Identify the blood parasite species.
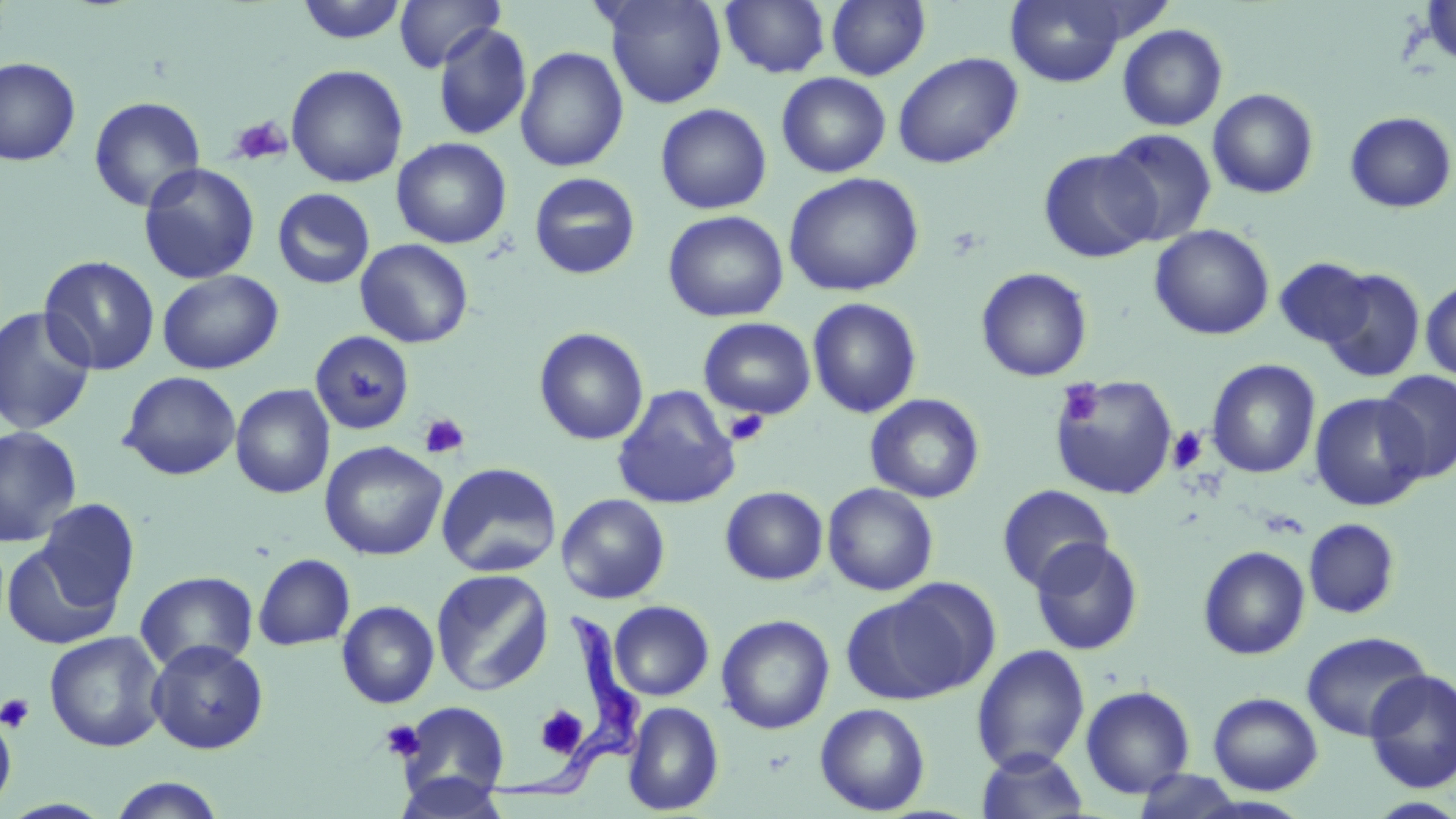

Trypanosoma brucei.

image size = 1456×819 pixels
magnification = 1000x
Trypanosoma brucei locations = approximate bounding boxes as (x1, y1, x2, y2) in pixels: (484, 610, 647, 804)
platelet locations = approximate bounding boxes as (x1, y1, x2, y2) in pixels: (227, 115, 292, 167), (1058, 380, 1104, 426), (724, 409, 770, 447), (418, 413, 469, 460), (1167, 427, 1208, 473), (0, 693, 36, 734), (535, 705, 588, 758), (380, 719, 426, 762)
stain = May-Grünwald-Giemsa
uninfected red blood cell locations = approximate bounding boxes as (x1, y1, x2, y2) in pixels: (394, 0, 504, 72), (601, 0, 728, 108), (720, 0, 831, 78), (826, 0, 930, 81), (1004, 0, 1130, 87), (1420, 0, 1456, 70), (295, 1, 409, 45), (432, 22, 532, 141), (1117, 24, 1228, 131), (515, 46, 629, 173), (893, 52, 1022, 169), (0, 57, 81, 166), (286, 64, 409, 188), (776, 72, 890, 178), (1207, 88, 1319, 199), (88, 95, 206, 212), (655, 103, 772, 215), (1343, 111, 1455, 213), (1102, 128, 1218, 246), (391, 137, 512, 249), (1038, 148, 1160, 263), (138, 162, 260, 284), (529, 172, 641, 280), (783, 172, 924, 297), (272, 188, 375, 290), (663, 210, 788, 323), (1150, 224, 1274, 340), (355, 239, 474, 348), (38, 255, 160, 375), (1274, 257, 1376, 349), (976, 267, 1092, 382), (1319, 268, 1427, 385), (158, 269, 282, 374), (1420, 280, 1456, 382), (807, 297, 923, 419), (0, 305, 96, 435), (698, 317, 816, 420), (533, 327, 649, 446), (308, 330, 415, 435), (1206, 359, 1321, 479), (118, 370, 241, 480), (1375, 371, 1456, 482), (1050, 375, 1178, 500), (230, 384, 335, 499), (611, 385, 741, 510), (1309, 392, 1429, 511), (865, 393, 985, 503), (0, 425, 82, 548), (320, 440, 448, 561), (436, 462, 562, 578), (823, 482, 939, 595), (996, 485, 1114, 593), (720, 486, 828, 585), (556, 493, 671, 604), (35, 498, 140, 612), (1303, 518, 1400, 619), (1029, 538, 1144, 655), (1, 541, 124, 651), (1198, 545, 1310, 659), (253, 553, 356, 651), (430, 568, 555, 696), (135, 570, 258, 674), (841, 585, 986, 704), (336, 600, 440, 709), (609, 600, 714, 701), (716, 614, 835, 735), (1301, 630, 1432, 742), (44, 631, 167, 753), (146, 639, 268, 754), (971, 644, 1090, 773), (1363, 669, 1456, 793), (1080, 685, 1195, 798), (1208, 692, 1323, 795), (397, 701, 511, 803), (622, 701, 725, 815), (814, 702, 930, 815), (0, 708, 16, 815), (976, 748, 1089, 819), (1129, 769, 1250, 817), (395, 772, 510, 818), (106, 777, 228, 818), (1364, 797, 1456, 818)
modality = optical microscopy
field of view = one of a larger specimen
preparation = thin blood smear